Give the position of every malaria parasite.
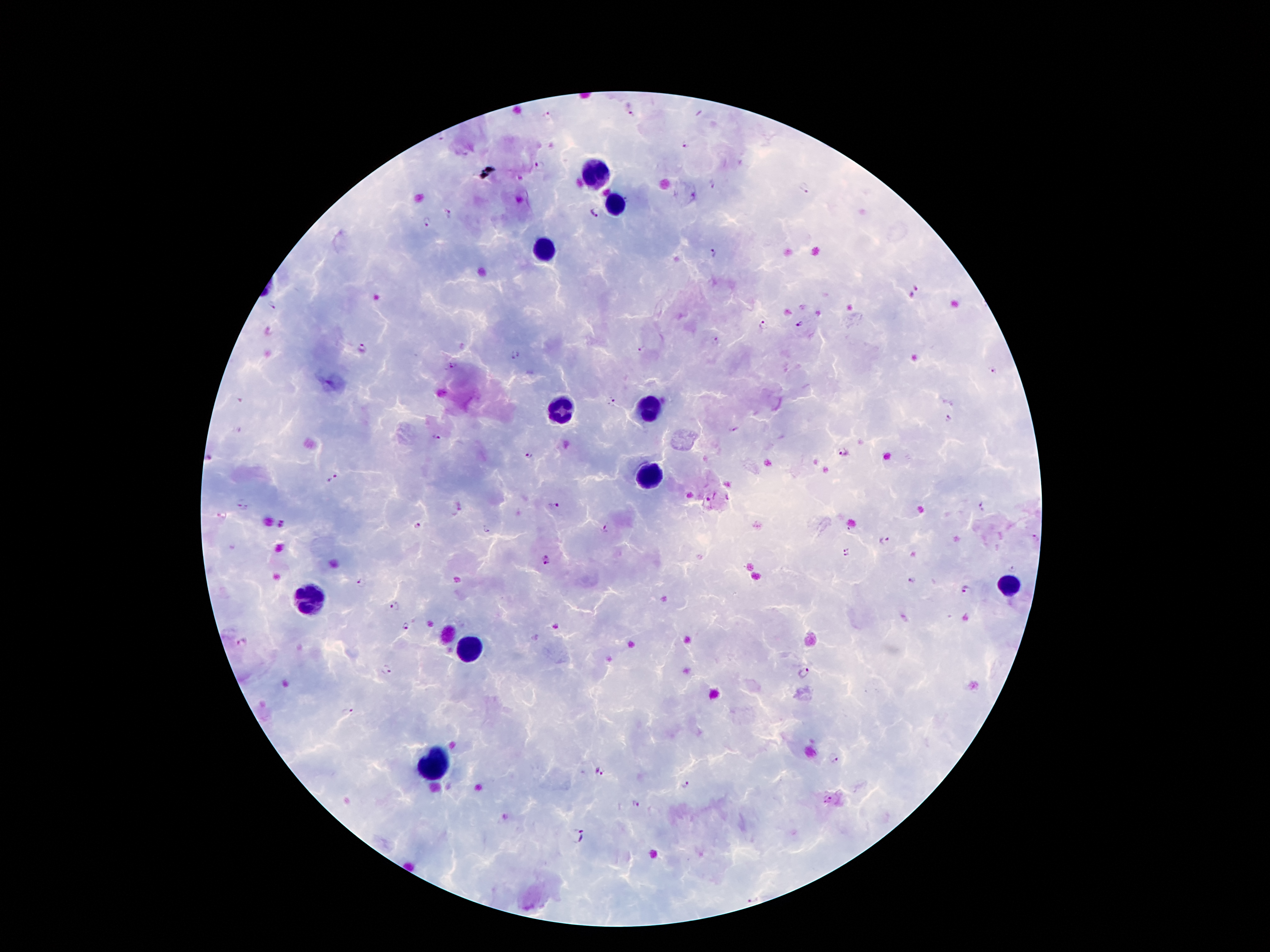
Approximate centers as {x, y} in pixels.
Malaria parasites: {632, 114}, {547, 115}, {442, 139}, {685, 147}, {539, 165}, {714, 185}, {804, 189}, {594, 213}, {449, 214}, {426, 222}, {713, 254}, {917, 289}, {271, 306}, {762, 325}, {800, 325}, {715, 341}, {361, 347}, {642, 351}, {515, 355}, {452, 365}, {992, 370}, {612, 403}, {948, 419}, {735, 429}, {436, 438}, {842, 453}, {528, 457}, {208, 459}, {332, 478}, {728, 498}, {554, 505}, {982, 506}, {242, 507}, {283, 525}, {418, 525}, {608, 528}, {486, 529}, {1035, 539}, {885, 542}, {847, 553}, {546, 560}, {1010, 568}, {912, 580}, {363, 583}, {967, 589}, {395, 606}, {406, 625}, {555, 627}, {241, 642}, {389, 669}, {804, 672}, {347, 712}, {835, 758}, {600, 771}, {687, 785}, {822, 799}, {832, 800}, {635, 803}, {577, 836}, {753, 896}.

Leukocyte locations: {596, 174}, {615, 207}, {544, 249}, {559, 409}, {648, 412}, {650, 478}, {1008, 586}, {309, 602}, {470, 651}, {433, 767}. Smartphone photograph taken through the microscope eyepiece. Thick peripheral-blood smear. Giemsa stain. 100x magnification. Image is 1270×952 pixels. One field from this slide. Patient malaria status: infected with Plasmodium falciparum.